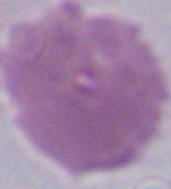
magnification = 1000x
identification = red blood cell
modality = photomicrograph